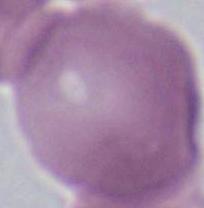

1000x magnification. Photomicrograph. An erythrocyte is shown.